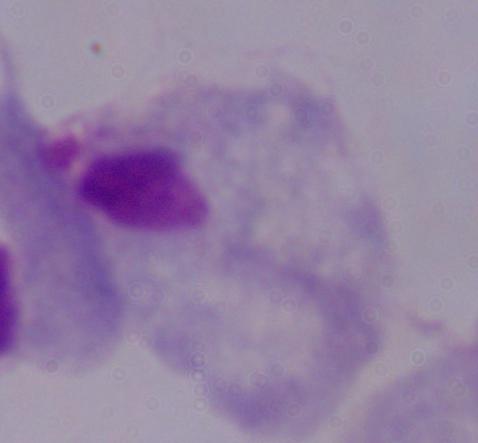

modality = micrograph
magnification = 1000x
identification = trichomonad